Locate and identify every blood parasite.
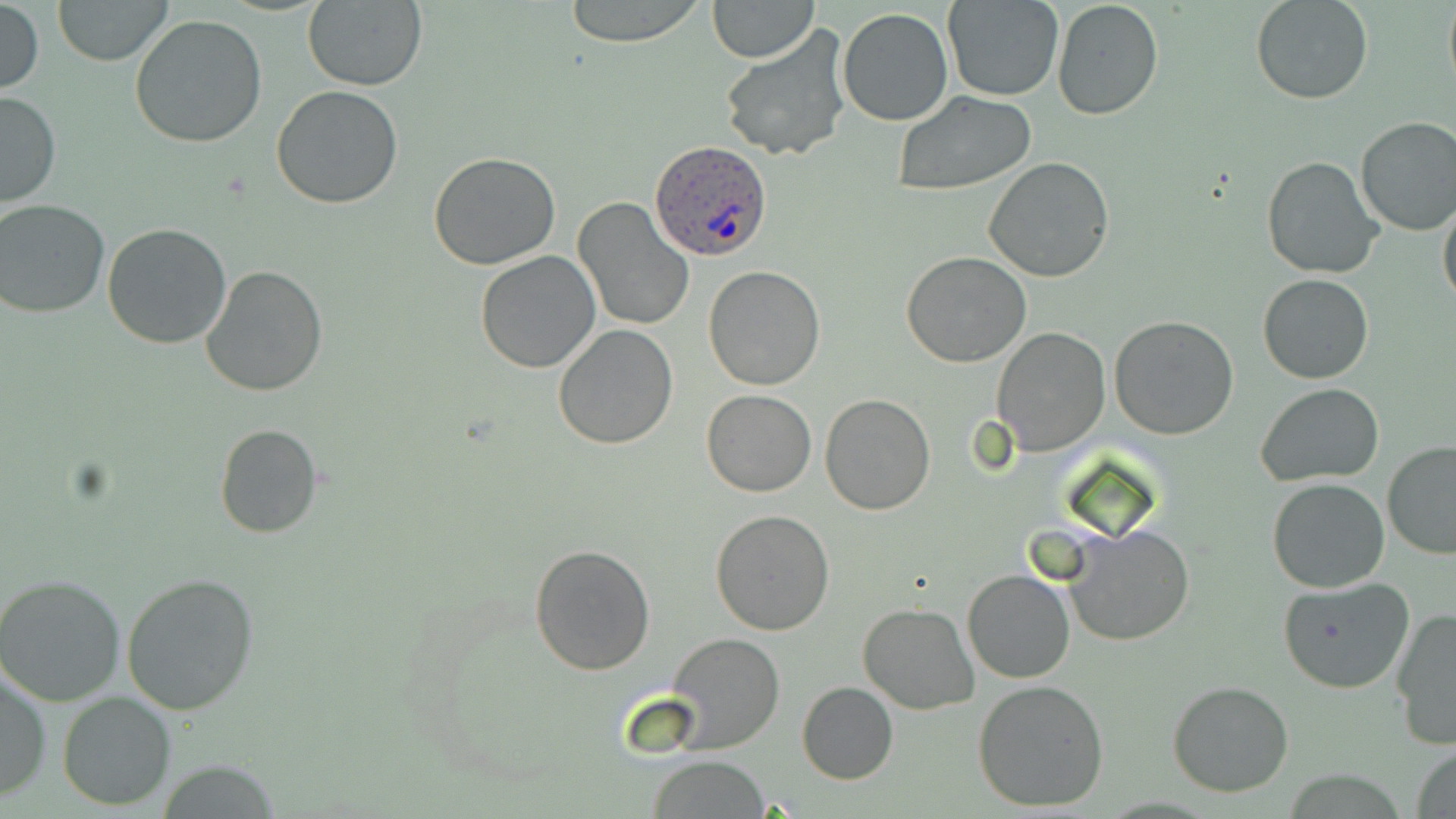

Approximate bounding boxes as (x1, y1, x2, y2) in pixels.
Plasmodium ovale-infected red blood cells: (650, 140, 771, 260).
No Plasmodium falciparum, Plasmodium malariae, Plasmodium vivax, Babesia divergens, or Trypanosoma brucei observed.

Uninfected red blood cell locations: (53, 0, 171, 65), (559, 0, 708, 46), (707, 0, 818, 63), (942, 0, 1064, 101), (1052, 0, 1164, 121), (1252, 0, 1372, 104), (1442, 0, 1456, 96), (1, 1, 45, 98), (302, 1, 427, 91), (837, 7, 953, 127), (129, 14, 267, 149), (717, 23, 856, 162), (271, 85, 404, 208), (0, 91, 61, 209), (893, 91, 1039, 197), (1353, 116, 1456, 236), (1265, 129, 1456, 260), (427, 152, 561, 270), (1260, 155, 1383, 279), (983, 158, 1115, 284), (572, 198, 694, 332), (1438, 198, 1456, 315), (1, 199, 114, 318), (103, 223, 233, 350), (474, 251, 603, 374), (902, 251, 1033, 368), (200, 266, 328, 396), (702, 266, 827, 391), (1258, 273, 1373, 384), (1109, 316, 1241, 440), (551, 323, 678, 450), (990, 325, 1110, 456), (1255, 383, 1385, 484), (700, 388, 817, 496), (819, 392, 936, 515), (214, 424, 323, 537), (1382, 440, 1456, 560), (1267, 477, 1390, 594), (711, 509, 835, 634), (1059, 524, 1196, 646), (529, 543, 656, 676), (962, 568, 1076, 684), (121, 571, 262, 714), (1, 572, 126, 705), (1278, 576, 1414, 694), (858, 602, 978, 714), (1391, 606, 1456, 749), (664, 633, 785, 754), (1, 666, 51, 803), (973, 680, 1109, 812), (1167, 681, 1295, 798), (797, 682, 898, 785), (57, 692, 176, 809), (1411, 744, 1456, 819), (647, 755, 769, 818), (154, 762, 284, 818). Slide-level diagnosis: Plasmodium ovale. Image is 1456×819 pixels. Thin blood smear. Optical microscopy. May-Grünwald-Giemsa stain. One field of a larger specimen. 1000x magnification.